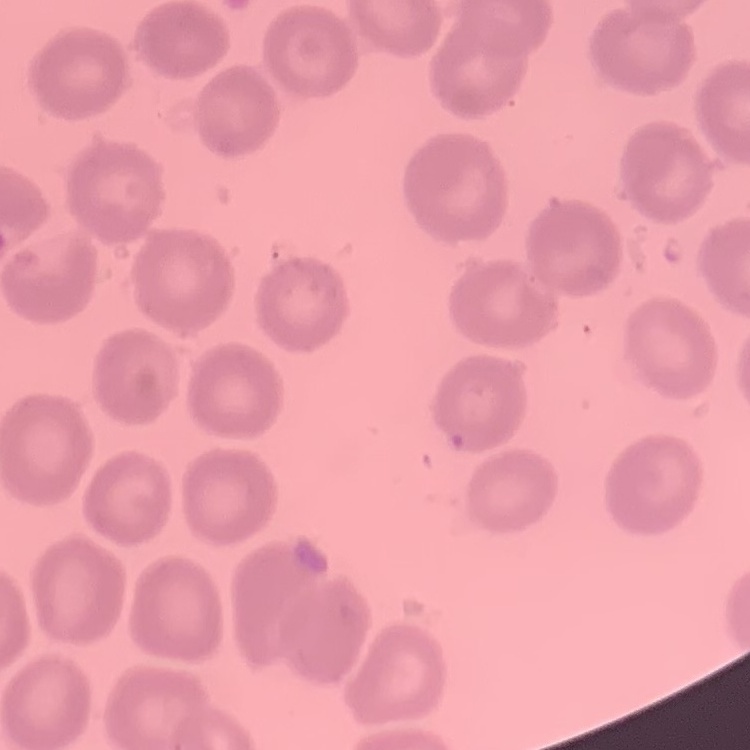
The erythrocytes show no rouleaux formation. Square crop of a larger photomicrograph. Stained with either Field's or Giemsa. Thin blood film.